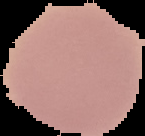
Image is 145×136 pixels. The area outside the segmented cell region is set to black. Malaria status: uninfected. From a thin blood film.